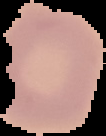
image type = cell region segmented out of the field of view; surrounding area masked to black
result = no malaria parasites seen
image size = 106×136 pixels
preparation = thin blood smear